Classify this cell by malaria status.
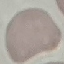

It is uninfected.

Summary:
  - Stain: Giemsa
  - Image type: cell patch, automatically extracted from a larger field of view and resized to 64 × 64 pixels
  - Capture: smartphone camera at the microscope eyepiece
  - Preparation: thin blood film